State the blood parasite species.
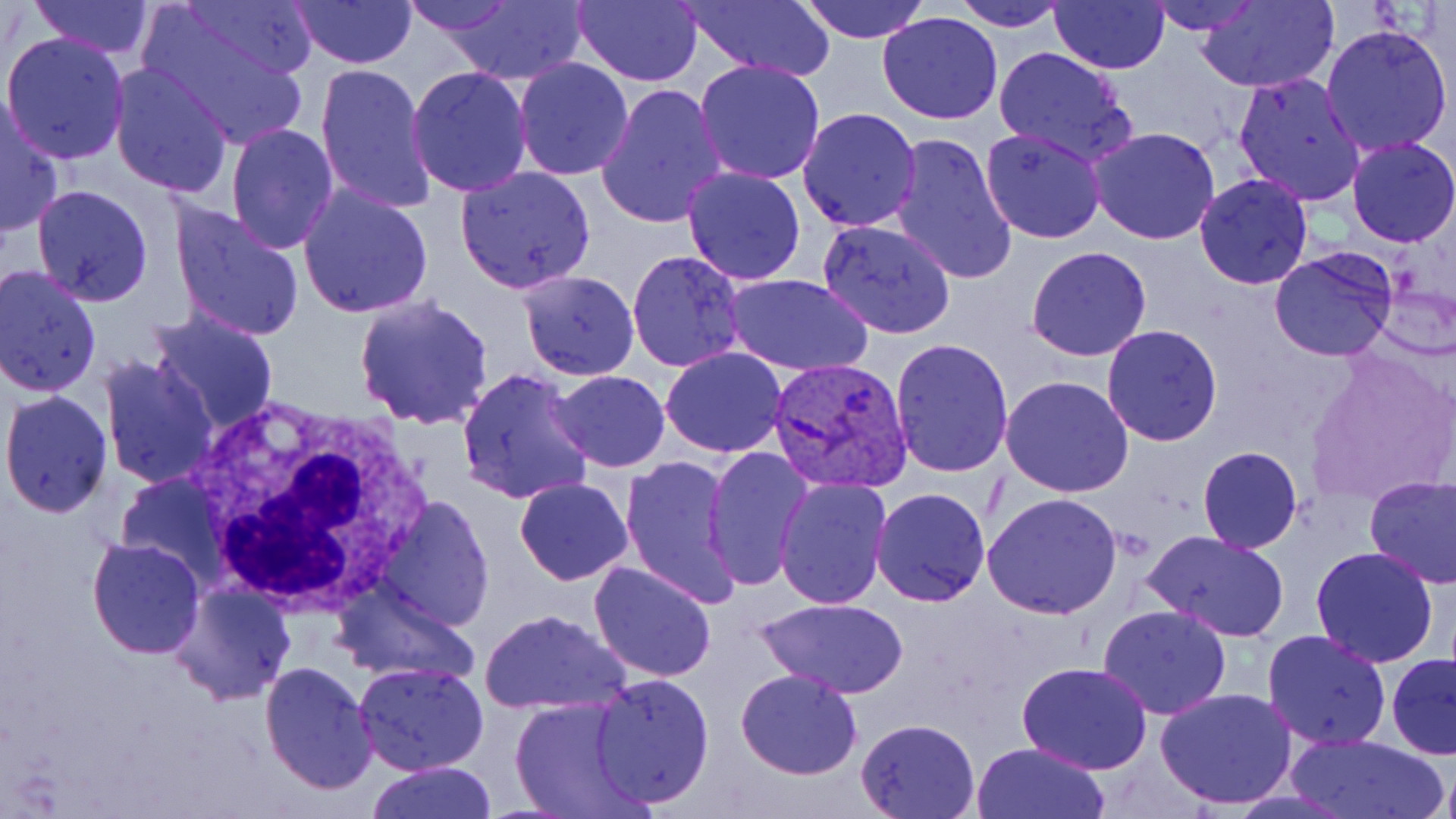

Plasmodium vivax.

Summary:
  - Coordinate format: approximate bounding boxes as named x1/y1/x2/y2 corners in pixels
  - White blood cell locations: (x1=179, y1=399, x2=433, y2=613)
  - Uninfected red blood cell locations: (x1=28, y1=0, x2=158, y2=59), (x1=178, y1=0, x2=321, y2=79), (x1=294, y1=0, x2=416, y2=68), (x1=397, y1=0, x2=517, y2=36), (x1=572, y1=0, x2=704, y2=86), (x1=675, y1=0, x2=837, y2=81), (x1=799, y1=0, x2=931, y2=43), (x1=953, y1=0, x2=1071, y2=29), (x1=1049, y1=0, x2=1169, y2=72), (x1=1145, y1=0, x2=1263, y2=34), (x1=1192, y1=0, x2=1340, y2=93), (x1=439, y1=1, x2=588, y2=87), (x1=142, y1=7, x2=313, y2=148), (x1=877, y1=12, x2=1005, y2=126), (x1=1320, y1=23, x2=1454, y2=159), (x1=2, y1=31, x2=130, y2=163), (x1=991, y1=47, x2=1137, y2=167), (x1=513, y1=57, x2=635, y2=181), (x1=694, y1=59, x2=826, y2=186), (x1=316, y1=61, x2=436, y2=215), (x1=108, y1=63, x2=235, y2=198), (x1=405, y1=65, x2=533, y2=197), (x1=1233, y1=73, x2=1367, y2=209), (x1=595, y1=84, x2=729, y2=231), (x1=0, y1=93, x2=66, y2=238), (x1=797, y1=107, x2=922, y2=232), (x1=226, y1=122, x2=339, y2=253), (x1=1089, y1=126, x2=1220, y2=245), (x1=979, y1=127, x2=1106, y2=244), (x1=891, y1=134, x2=1018, y2=288), (x1=1346, y1=136, x2=1456, y2=246), (x1=456, y1=165, x2=596, y2=293), (x1=680, y1=165, x2=807, y2=285), (x1=1192, y1=174, x2=1315, y2=291), (x1=298, y1=182, x2=434, y2=319), (x1=31, y1=185, x2=154, y2=307), (x1=170, y1=199, x2=304, y2=342), (x1=817, y1=216, x2=958, y2=340), (x1=1024, y1=246, x2=1153, y2=363), (x1=1269, y1=247, x2=1398, y2=362), (x1=626, y1=250, x2=747, y2=373), (x1=0, y1=264, x2=100, y2=397), (x1=516, y1=269, x2=639, y2=380), (x1=726, y1=274, x2=874, y2=378), (x1=351, y1=293, x2=496, y2=429), (x1=146, y1=309, x2=282, y2=436), (x1=1100, y1=325, x2=1223, y2=445), (x1=891, y1=337, x2=1015, y2=476), (x1=660, y1=347, x2=786, y2=458), (x1=97, y1=353, x2=218, y2=489), (x1=456, y1=366, x2=592, y2=507), (x1=550, y1=370, x2=670, y2=472), (x1=999, y1=376, x2=1134, y2=499), (x1=1, y1=389, x2=115, y2=518), (x1=701, y1=445, x2=814, y2=589), (x1=1198, y1=445, x2=1302, y2=552), (x1=620, y1=454, x2=739, y2=603), (x1=116, y1=473, x2=228, y2=585), (x1=1364, y1=475, x2=1456, y2=588), (x1=773, y1=476, x2=892, y2=611), (x1=513, y1=477, x2=635, y2=586), (x1=871, y1=487, x2=992, y2=606), (x1=981, y1=493, x2=1124, y2=619), (x1=377, y1=495, x2=493, y2=631), (x1=1141, y1=528, x2=1291, y2=642), (x1=86, y1=536, x2=205, y2=658), (x1=1310, y1=545, x2=1440, y2=667), (x1=586, y1=560, x2=717, y2=682), (x1=331, y1=582, x2=481, y2=688), (x1=170, y1=583, x2=297, y2=706), (x1=755, y1=597, x2=910, y2=699), (x1=1097, y1=604, x2=1231, y2=719), (x1=480, y1=607, x2=629, y2=715), (x1=1262, y1=630, x2=1392, y2=749), (x1=1386, y1=652, x2=1456, y2=759), (x1=259, y1=661, x2=377, y2=795), (x1=1016, y1=661, x2=1153, y2=773), (x1=354, y1=662, x2=491, y2=777), (x1=735, y1=668, x2=863, y2=779), (x1=588, y1=673, x2=715, y2=808), (x1=1154, y1=687, x2=1299, y2=809), (x1=509, y1=698, x2=651, y2=819), (x1=854, y1=717, x2=982, y2=818), (x1=1285, y1=733, x2=1447, y2=818), (x1=972, y1=742, x2=1110, y2=819), (x1=365, y1=761, x2=497, y2=818), (x1=1436, y1=763, x2=1456, y2=819)
  - Plasmodium vivax-infected red blood cell locations: (x1=768, y1=356, x2=912, y2=493)
  - Modality: optical microscopy
  - Field of view: single
  - Magnification: 1000x
  - Stain: May-Grünwald-Giemsa
  - Preparation: thin blood smear
  - Image size: 1456×819 pixels